Report the malaria status of this cell.
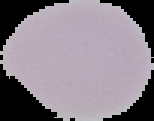

It is uninfected.

Summary:
  - Image type: segmented cell region on a black background
  - Image size: 154×121 pixels
  - Preparation: thin blood film